Assess the morphology of the red blood cells.
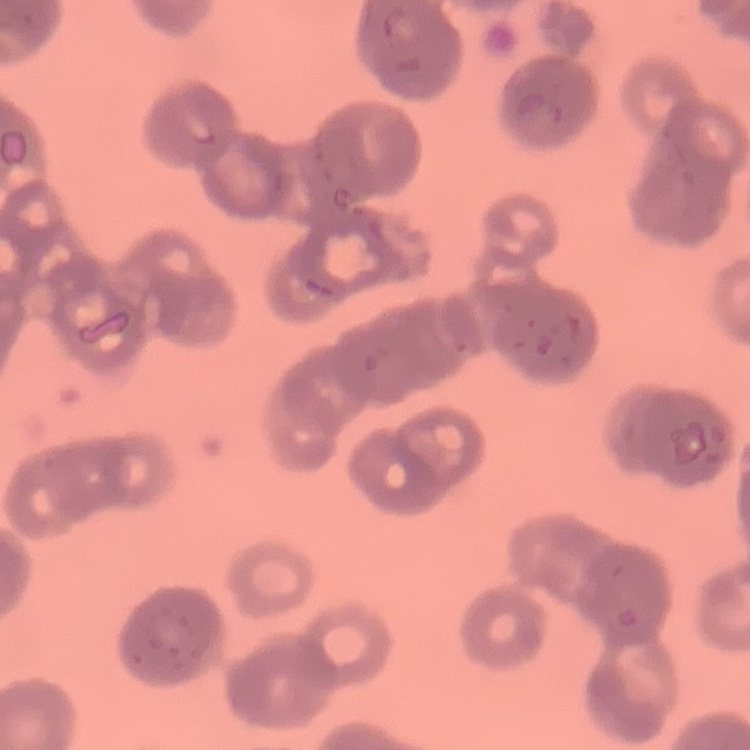

They show rouleaux formation.

Summary:
  - Preparation: thin blood film
  - Stain: Field's or Giemsa
  - Image type: square crop of a larger photomicrograph